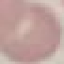
Summary:
  - Result: no malaria parasites seen
  - Stain: Giemsa
  - Capture: smartphone through the microscope eyepiece
  - Preparation: thin blood film
  - Image type: cell patch, automatically extracted from a larger field of view and resized to 64 × 64 pixels